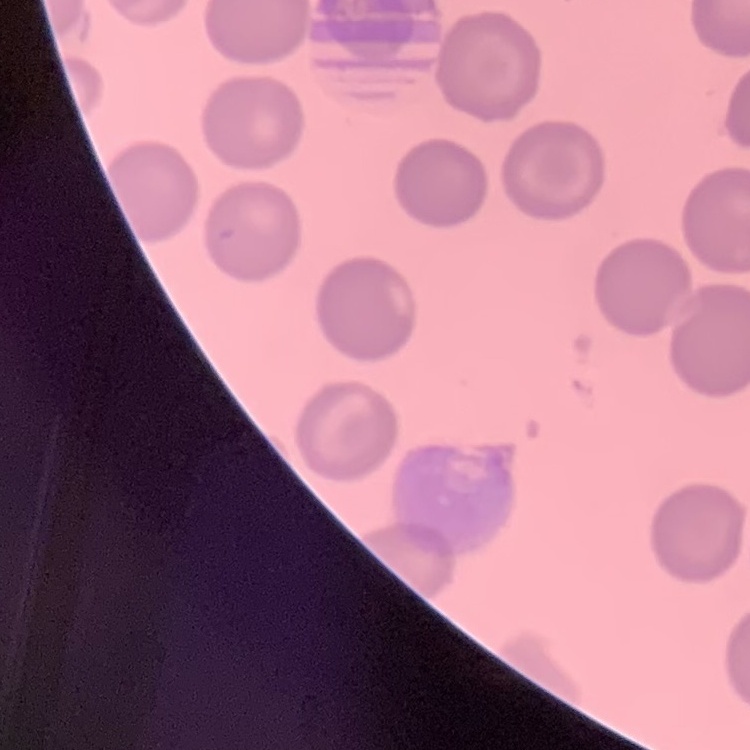
Summary:
  - Erythrocyte morphology: no rouleaux formation
  - Image type: square crop of a larger photomicrograph
  - Preparation: thin peripheral smear
  - Stain: Field's or Giemsa